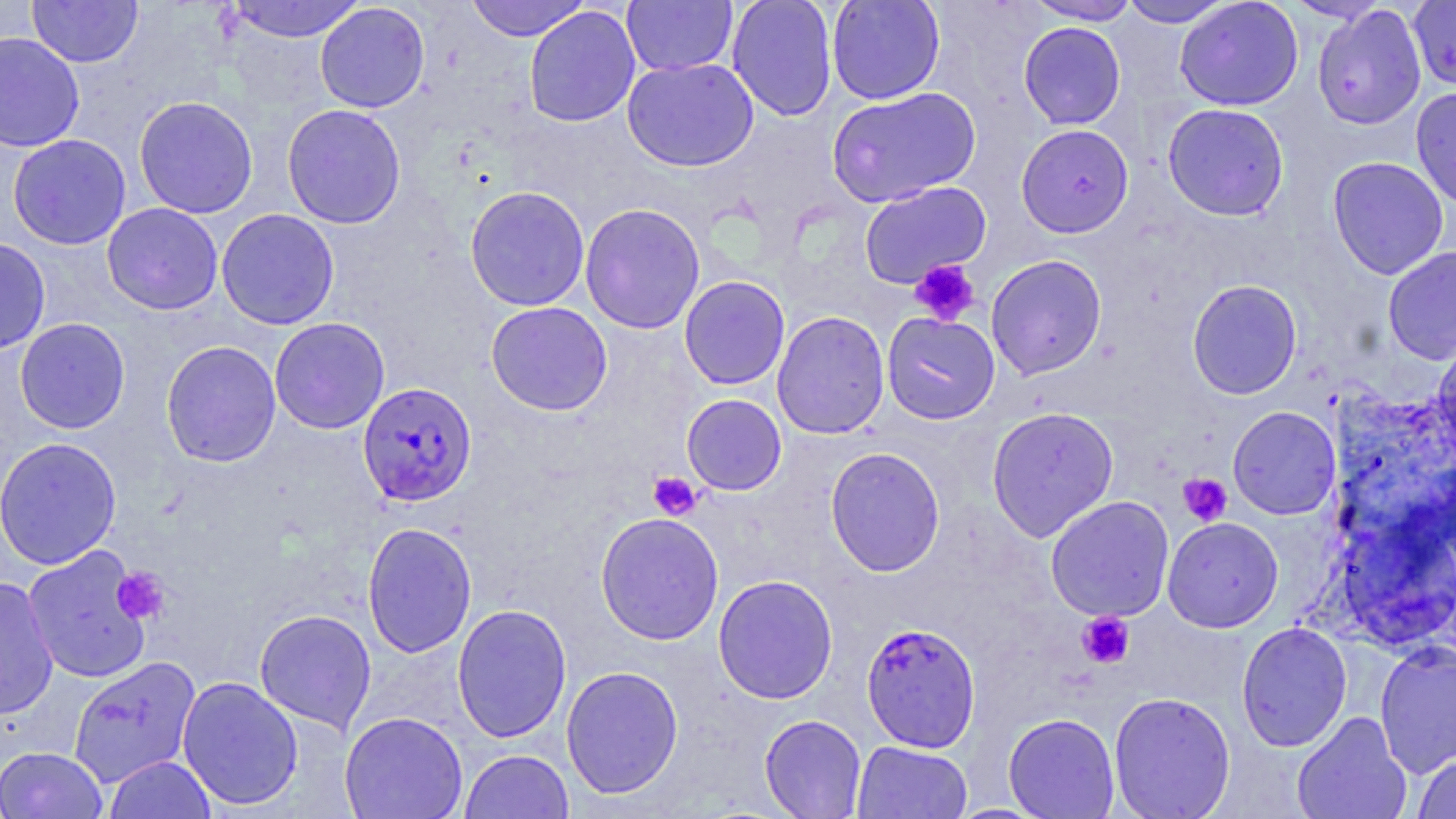

{
  "slide_level_diagnosis": "Plasmodium falciparum",
  "preparation": "thin blood film",
  "stain": "May-Grünwald-Giemsa",
  "magnification": "1000x",
  "image_size": "1456×819 pixels",
  "modality": "optical microscopy",
  "uninfected_red_blood_cell_locations": "approximate bounding boxes as (x1,y1)-(x2,y2) corner pairs in pixels: (27,0)-(143,67), (223,0)-(367,43), (465,0)-(590,41), (727,0)-(838,121), (826,0)-(945,105), (1024,0)-(1142,25), (1118,0)-(1237,28), (1174,0)-(1304,111), (620,1)-(738,76), (1408,1)-(1456,91), (315,3)-(430,113), (1312,5)-(1426,130), (523,6)-(641,127), (1018,21)-(1126,129), (0,31)-(85,153), (622,57)-(759,172), (826,86)-(981,208), (1411,86)-(1456,211), (133,96)-(258,218), (1162,102)-(1289,221), (282,103)-(406,229), (1016,123)-(1134,238), (7,134)-(131,250), (1327,156)-(1450,280), (859,181)-(992,288), (465,185)-(590,311), (102,202)-(223,315), (580,203)-(705,334), (216,209)-(340,330), (0,237)-(50,354), (1382,246)-(1456,364), (986,254)-(1107,380), (679,275)-(790,390), (1186,279)-(1303,399), (486,301)-(613,416), (771,310)-(890,439), (881,311)-(1001,425), (14,317)-(130,434), (269,317)-(390,434), (1432,333)-(1456,466), (160,340)-(281,467), (681,394)-(787,495), (986,406)-(1119,543), (1227,406)-(1341,519), (0,436)-(122,570), (825,446)-(946,577), (1045,495)-(1174,621), (595,512)-(725,645), (1162,517)-(1283,632), (361,522)-(477,658), (22,545)-(153,684), (712,574)-(838,704), (0,576)-(59,721), (452,603)-(573,742), (254,609)-(377,734), (1236,622)-(1352,751), (1374,641)-(1456,778), (68,656)-(201,787), (561,665)-(684,798), (177,675)-(304,810), (1108,691)-(1236,819), (339,711)-(468,819), (1292,711)-(1413,819), (1003,712)-(1120,818), (759,714)-(867,818), (851,741)-(973,819), (0,745)-(108,819), (459,749)-(574,819), (1411,753)-(1455,819), (104,755)-(216,819)",
  "plasmodium_falciparum_infected_red_blood_cell_locations": "approximate bounding boxes as (x1,y1)-(x2,y2) corner pairs in pixels: (357,381)-(477,507), (861,622)-(981,752)",
  "platelet_locations": "approximate bounding boxes as (x1,y1)-(x2,y2) corner pairs in pixels: (909,259)-(980,326), (647,471)-(701,520), (1178,473)-(1232,526), (111,567)-(170,624), (1076,611)-(1135,669)",
  "field_of_view": "single"
}